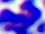

modality = photomicrograph
identification = leukocyte
magnification = 400x